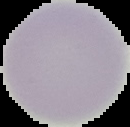

Summary:
  - Result: no Plasmodium parasites detected
  - Preparation: thin blood smear
  - Image type: segmented cell region with the area outside set to black
  - Image size: 130×127 pixels